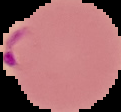

malaria status = parasitized
image type = segmented cell region on a black background
preparation = thin blood film
image size = 121×112 pixels